State which parasite is depicted.
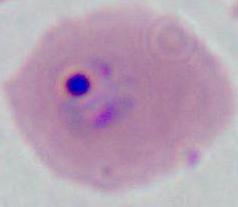
This is Plasmodium.

Captured at either 400x or 1000x magnification. Micrograph.